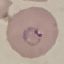

result = malaria parasites detected
stain = Giemsa
preparation = thin blood smear
image type = automatically extracted cell patch, resized to 64 × 64 pixels
capture = smartphone camera at the microscope eyepiece